Outline every leukocyte.
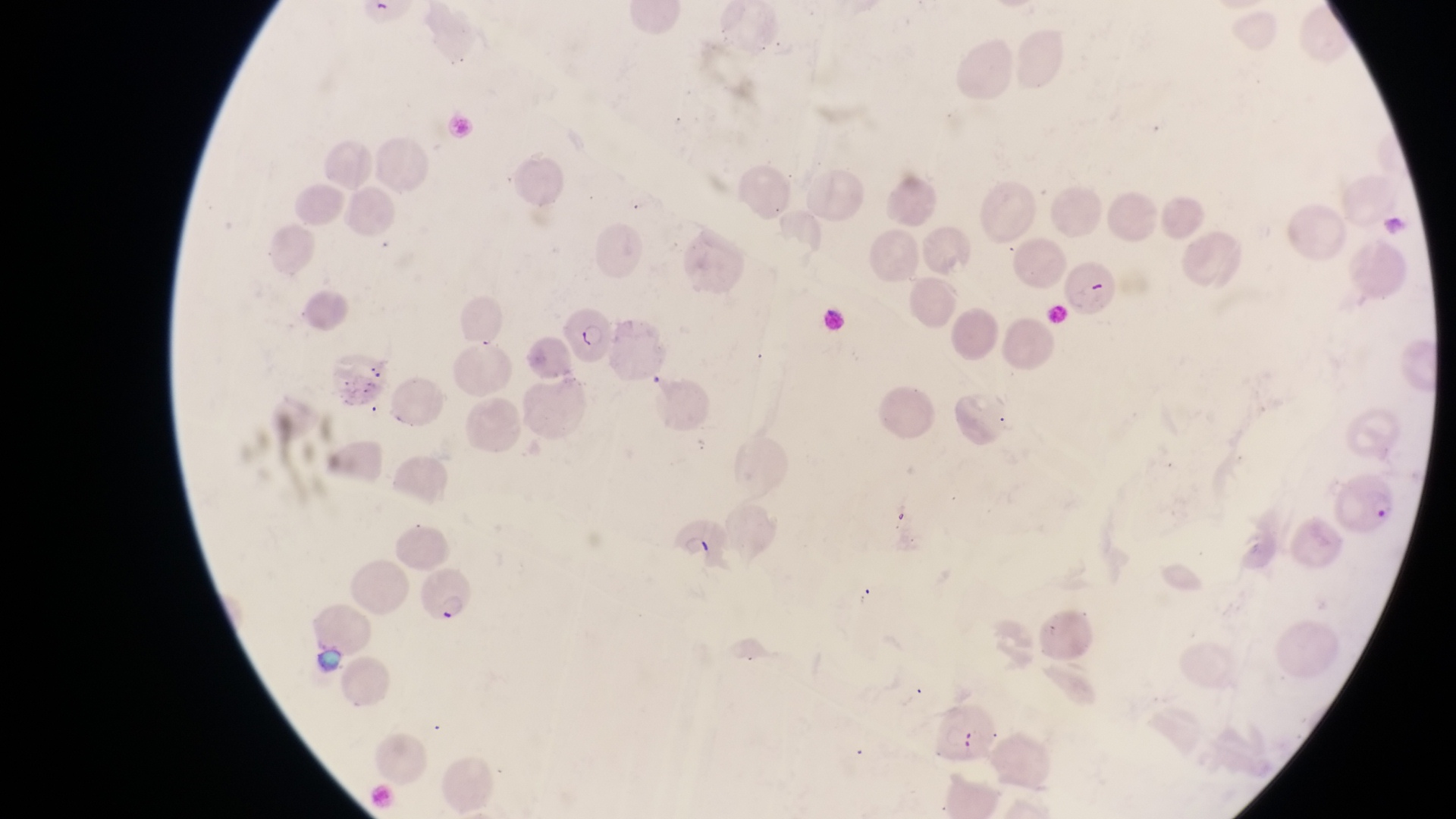
No leukocytes observed.

Approximate bounding boxes as {left, top, right, bottom} in pixels. Parasitised red blood cell locations: {1063, 258, 1121, 322}, {554, 304, 613, 363}, {1330, 470, 1401, 536}, {661, 513, 724, 565}, {420, 576, 484, 622}. Collected in Uganda. Thin blood film. At a magnification of 1000x. Photographed through the eyepiece of an Olympus CX-23 microscope with a smartphone camera. Image is 1456×819 pixels. Single field of view.